Assess this cell for malaria.
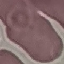

Uninfected.

Summary:
  - Capture: smartphone camera at the microscope eyepiece
  - Image type: cell patch, automatically extracted from a larger field of view and resized to 64 × 64 pixels
  - Preparation: thin blood film
  - Stain: Giemsa